Give the extent of all Plasmodium vivax-infected red blood cells.
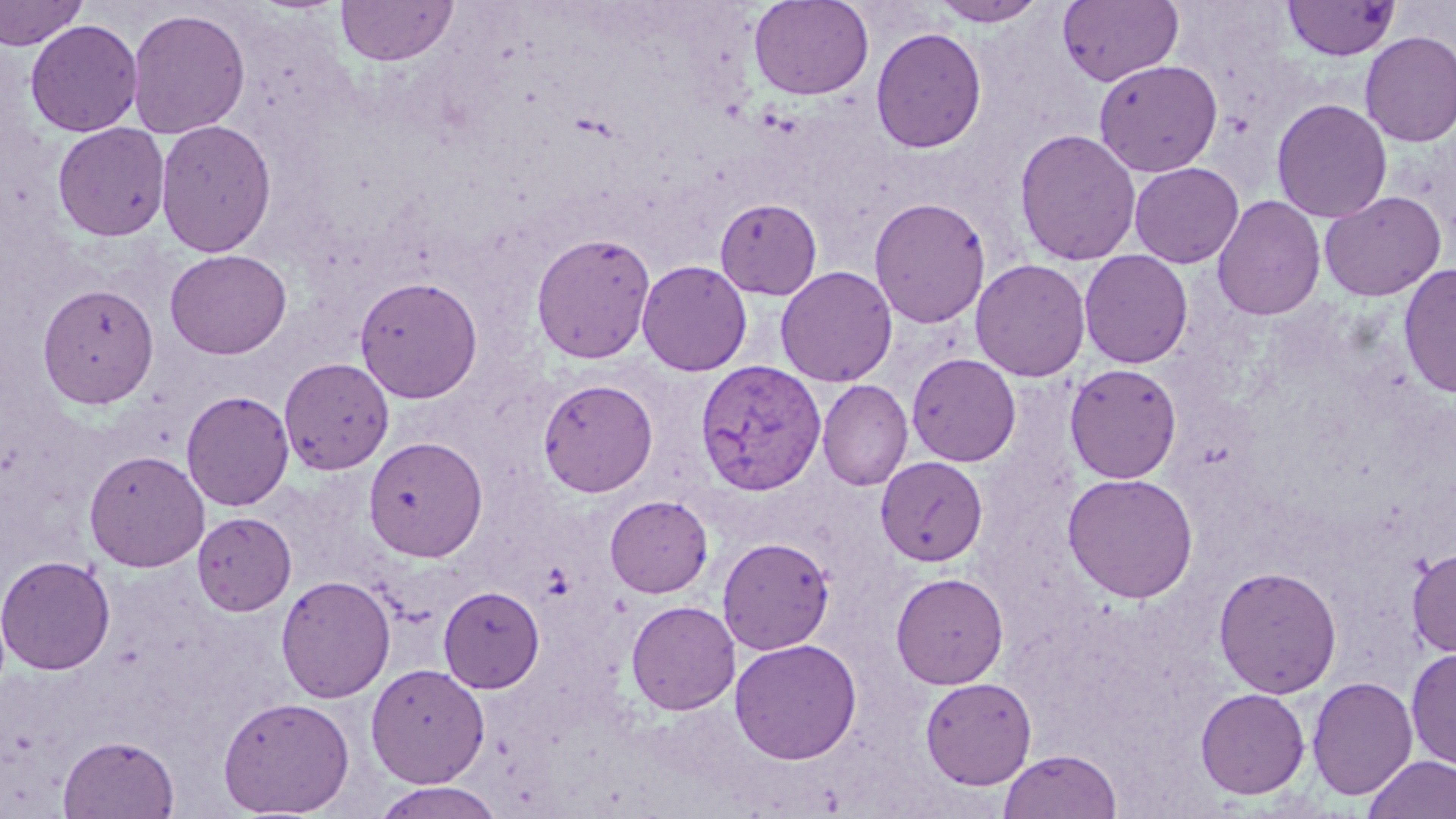
Approximate bounding boxes as (x1, y1, x2, y2) in pixels.
Plasmodium vivax-infected red blood cells: (694, 359, 826, 495).

Uninfected red blood cell locations: (0, 0, 89, 51), (335, 0, 458, 66), (749, 0, 874, 100), (1057, 0, 1184, 87), (930, 1, 1047, 27), (1282, 1, 1400, 61), (127, 7, 251, 139), (25, 19, 143, 137), (870, 26, 987, 154), (1359, 30, 1456, 147), (1093, 59, 1223, 177), (1270, 97, 1393, 223), (155, 119, 277, 257), (52, 122, 171, 242), (1013, 127, 1141, 266), (1297, 130, 1422, 292), (1129, 162, 1244, 268), (1319, 190, 1446, 301), (1211, 195, 1326, 321), (869, 196, 991, 327), (714, 198, 823, 300), (531, 231, 656, 364), (165, 249, 292, 359), (1079, 250, 1193, 369), (970, 258, 1091, 381), (636, 260, 752, 376), (1398, 263, 1456, 399), (775, 265, 897, 387), (354, 275, 483, 403), (36, 284, 158, 409), (906, 353, 1021, 466), (279, 357, 394, 475), (1064, 363, 1182, 484), (538, 378, 658, 497), (817, 380, 913, 491), (181, 389, 295, 511), (363, 436, 488, 562), (83, 449, 210, 572), (876, 456, 988, 567), (1062, 473, 1199, 602), (605, 494, 713, 598), (192, 511, 297, 616), (718, 537, 836, 655), (1407, 546, 1456, 657), (0, 554, 116, 675), (1212, 566, 1343, 699), (889, 572, 1009, 689), (275, 574, 396, 703), (438, 585, 545, 693), (625, 600, 740, 715), (730, 639, 862, 764), (1405, 647, 1456, 771), (365, 662, 491, 787), (919, 676, 1037, 789), (1307, 676, 1418, 800), (1194, 687, 1311, 800), (217, 695, 356, 817), (57, 734, 180, 818), (997, 748, 1123, 818), (1362, 754, 1456, 819), (370, 781, 508, 819). Slide-level diagnosis: Plasmodium vivax. Captured at 1000x magnification. May-Grünwald-Giemsa-stained preparation. One field of a larger specimen. Image is 1456×819 pixels. Thin blood film. Optical microscopy.